Report the malaria status of this cell.
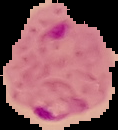

Parasitized.

Image is 118×130 pixels. From a thin blood film. Cell region segmented out of the field of view; the surrounding area is masked to black.